Assess this cell for malaria.
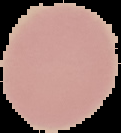

It is uninfected.

image type = segmented cell region with the area outside set to black
image size = 121×133 pixels
preparation = thin blood smear